Identify the parasite.
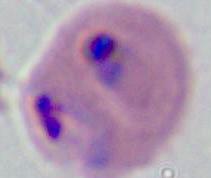
This is Plasmodium.

Captured at either 400x or 1000x magnification. Photomicrograph.